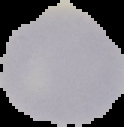 Result: negative for malaria parasites. From a thin blood smear. Segmented cell region on a black background. Image is 124×127 pixels.